Outline each Plasmodium malariae-infected red blood cell.
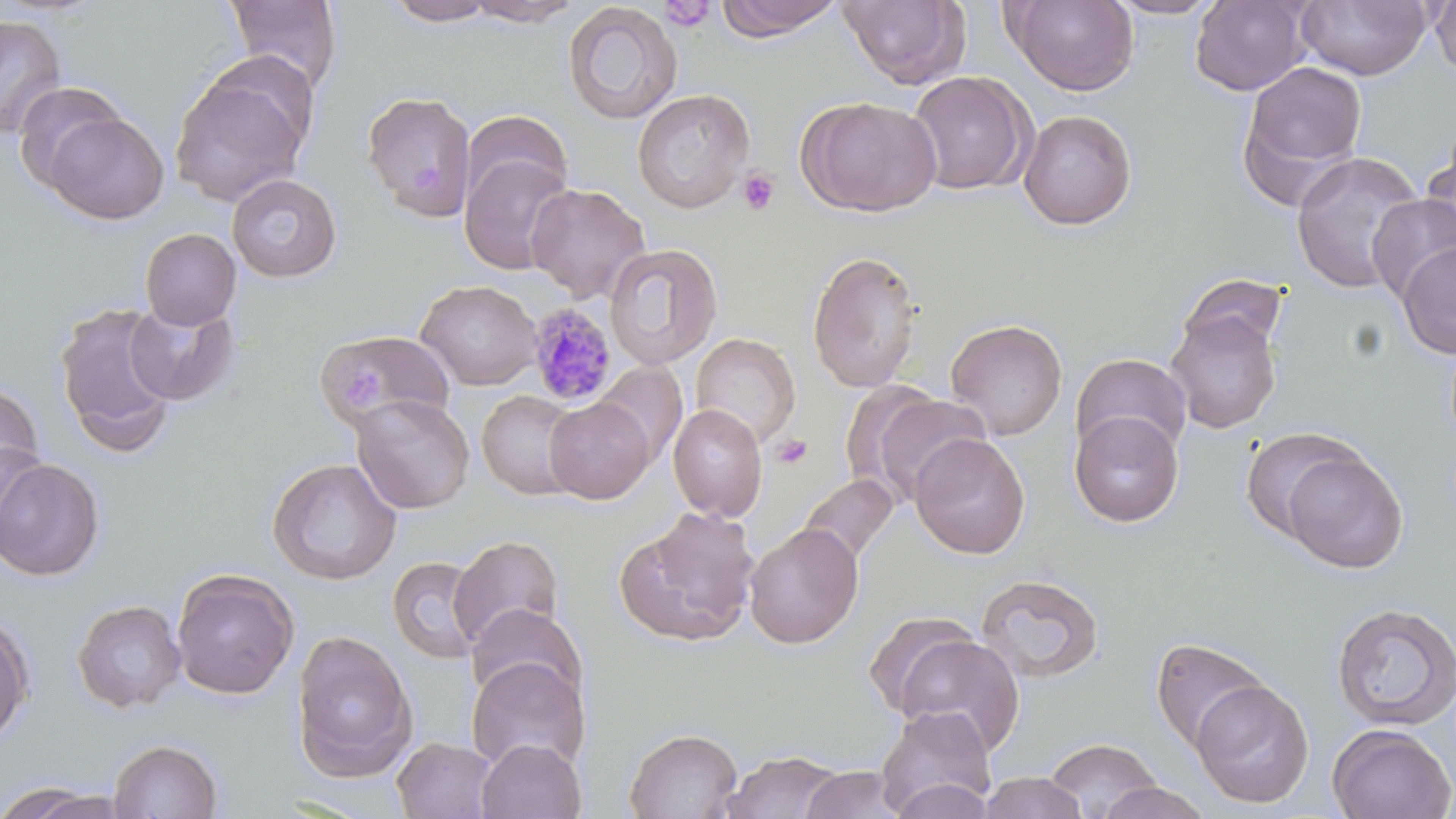
Approximate bounding boxes as (x1,y1)-(x2,y2) corner pairs in pixels.
Plasmodium malariae-infected red blood cells: (526,302)-(618,406).

Platelet locations: (659,1)-(715,32), (737,167)-(781,216), (770,435)-(813,469). Uninfected red blood cell locations: (223,0)-(344,92), (381,0)-(501,26), (464,0)-(585,26), (715,0)-(844,41), (837,0)-(971,89), (1003,0)-(1139,95), (1104,0)-(1227,19), (1189,0)-(1312,96), (1429,0)-(1456,81), (1295,1)-(1431,80), (561,3)-(683,125), (0,13)-(67,140), (1238,59)-(1369,199), (907,71)-(1033,195), (168,72)-(310,207), (13,81)-(128,190), (632,88)-(755,213), (362,91)-(477,221), (797,95)-(943,217), (460,109)-(573,209), (1018,109)-(1138,231), (45,112)-(169,225), (1420,139)-(1456,261), (1290,151)-(1425,295), (459,152)-(576,276), (226,173)-(342,282), (525,183)-(651,303), (1366,192)-(1456,303), (140,228)-(241,329), (1396,240)-(1456,359), (603,243)-(723,369), (807,249)-(922,393), (416,279)-(541,390), (123,299)-(241,406), (53,302)-(179,455), (1165,304)-(1284,434), (945,317)-(1068,441), (316,330)-(455,429), (690,332)-(801,449), (1070,353)-(1192,460), (592,362)-(687,469), (0,379)-(45,503), (476,390)-(581,500), (863,391)-(993,505), (350,394)-(475,514), (543,397)-(654,504), (668,403)-(768,521), (1069,410)-(1184,527), (1239,425)-(1367,544), (909,433)-(1031,559), (0,443)-(44,556), (1279,449)-(1408,573), (0,456)-(105,582), (266,457)-(402,585), (797,474)-(899,567), (615,507)-(761,648), (744,522)-(864,649), (448,534)-(565,652), (387,556)-(486,665), (171,568)-(299,700), (975,573)-(1105,683), (72,599)-(186,713), (1331,602)-(1456,731), (465,604)-(587,707), (0,609)-(35,746), (862,610)-(982,719), (291,629)-(417,782), (895,634)-(1025,755), (1150,637)-(1271,753), (466,656)-(589,774), (1189,679)-(1314,807), (875,706)-(997,816), (1327,724)-(1455,819), (624,727)-(743,819), (392,736)-(498,819), (1043,737)-(1163,818), (108,738)-(224,818), (476,738)-(585,819), (719,749)-(846,819), (799,766)-(909,818), (978,771)-(1088,819), (888,777)-(995,819), (1096,781)-(1215,819), (3,783)-(125,819). Slide-level diagnosis: Plasmodium malariae. 1000x magnification. May-Grünwald-Giemsa stain. Single field of view. Image is 1456×819 pixels. Thin blood smear. Light microscopy.